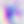
magnification = 400x
modality = photomicrograph
identification = Toxoplasma gondii